State which parasite is depicted.
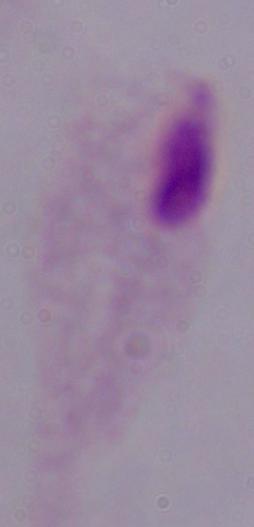
A trichomonad.

1000x magnification. Micrograph.